Classify this cell by malaria status.
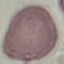

It is uninfected.

Automatically extracted cell patch, resized to 64 × 64 pixels. Giemsa stain. Thin blood film. Photographed with a smartphone camera at the microscope eyepiece.